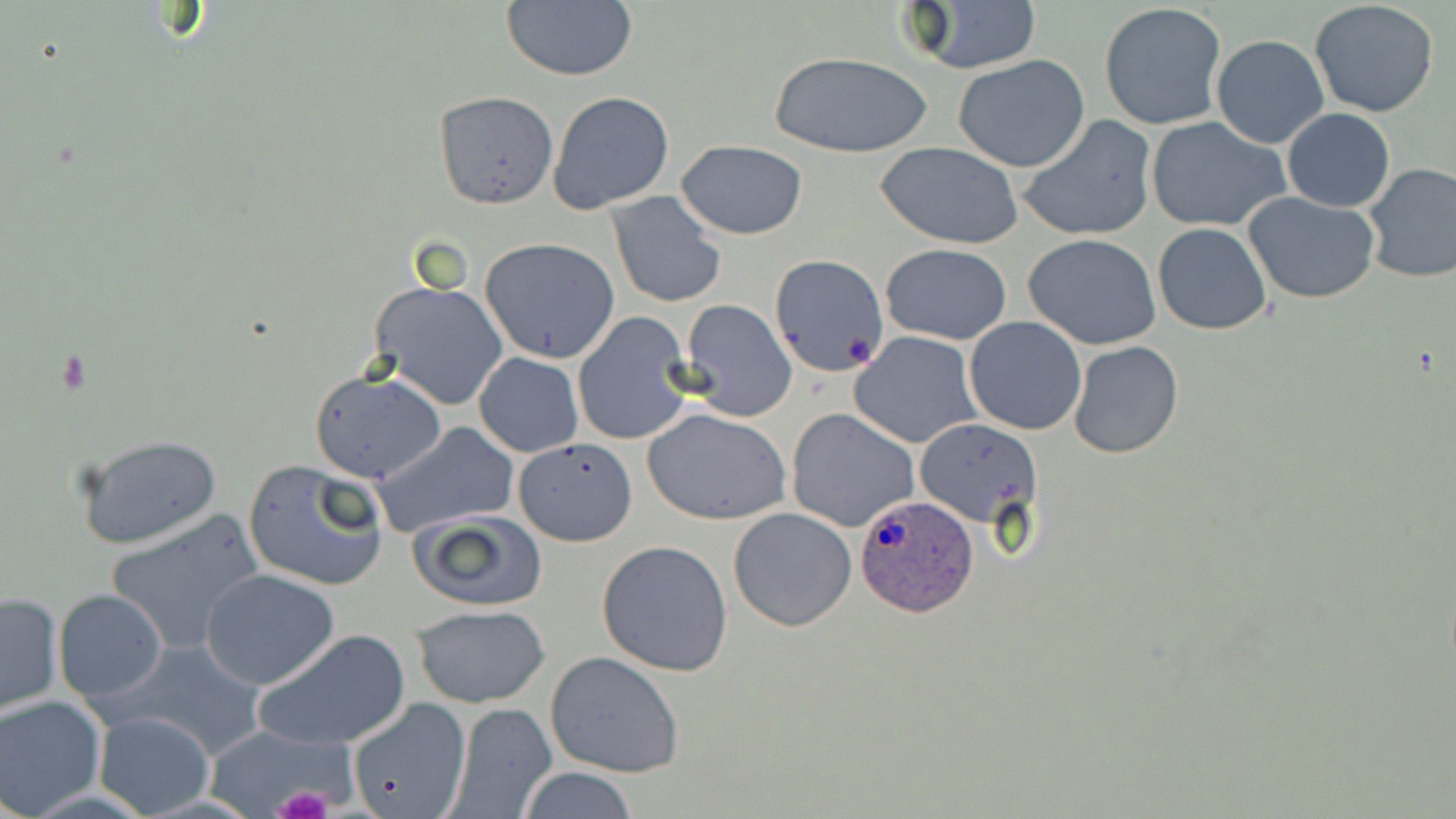
Approximate bounding boxes as (x1, y1, x2, y2) in pixels. Platelet locations: (272, 785, 335, 819). Plasmodium ovale-infected red blood cell locations: (855, 494, 979, 617). Uninfected red blood cell locations: (501, 0, 638, 82), (902, 2, 1043, 75), (1309, 2, 1440, 117), (1099, 3, 1226, 131), (1211, 35, 1329, 150), (771, 52, 931, 160), (954, 54, 1089, 172), (548, 90, 675, 213), (433, 91, 558, 208), (1283, 109, 1395, 212), (1016, 115, 1157, 243), (1146, 117, 1288, 232), (676, 140, 808, 239), (877, 141, 1025, 249), (1362, 162, 1456, 283), (605, 191, 727, 310), (1243, 193, 1380, 305), (1152, 223, 1273, 334), (1023, 234, 1164, 351), (480, 237, 621, 363), (880, 244, 1012, 345), (769, 253, 890, 378), (370, 280, 508, 411), (678, 300, 797, 421), (573, 313, 695, 445), (965, 317, 1087, 436), (850, 331, 982, 449), (1068, 341, 1182, 459), (474, 353, 584, 457), (308, 366, 445, 484), (787, 407, 918, 532), (644, 409, 790, 525), (916, 418, 1040, 529), (372, 422, 520, 537), (74, 431, 225, 553), (516, 436, 638, 547), (243, 458, 390, 592), (728, 507, 857, 630), (106, 508, 264, 655), (409, 509, 549, 612), (596, 539, 734, 675), (202, 568, 339, 689), (54, 590, 167, 703), (0, 591, 64, 715), (414, 604, 549, 708), (256, 628, 411, 751), (114, 639, 268, 760), (545, 651, 684, 778), (0, 694, 105, 817), (345, 701, 504, 819), (446, 702, 557, 818), (92, 710, 215, 817), (206, 725, 346, 815), (518, 766, 637, 819). Slide-level diagnosis: Plasmodium ovale. Optical microscopy. May-Grünwald-Giemsa-stained preparation. Captured at 1000x magnification. One field of a larger specimen. Image is 1456×819 pixels. Thin blood smear.